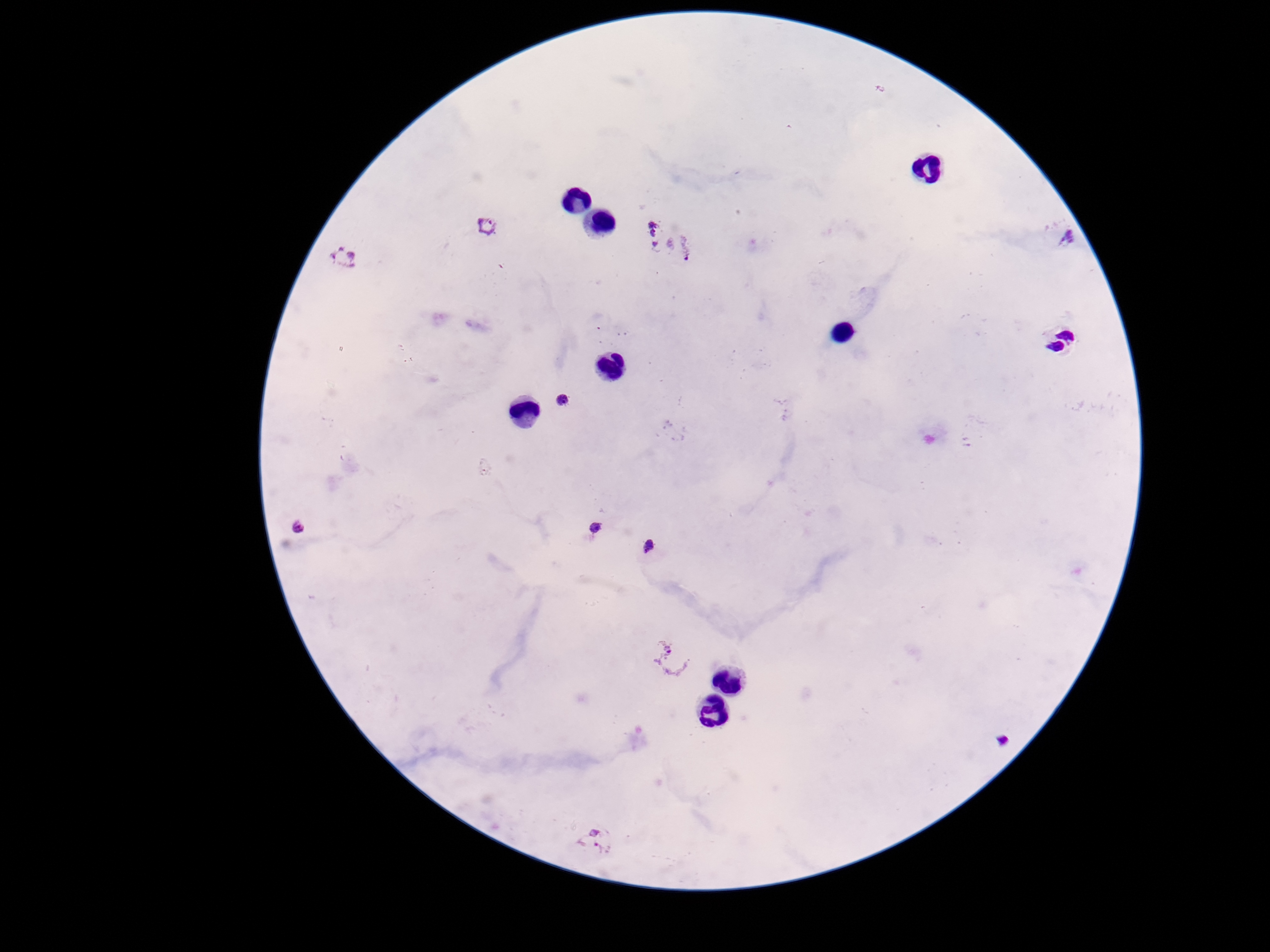

Approximate centers as [x, y] in pixels.
Summary:
  - Plasmodium parasite locations: [484, 229], [649, 230], [1068, 239], [687, 247], [342, 257], [567, 402], [297, 528], [598, 529], [649, 548], [678, 660], [1000, 735], [596, 842]
  - Capture: smartphone camera through the microscope eyepiece
  - Magnification: 100x
  - Preparation: thick blood smear
  - Field of view: one from this slide
  - Stain: Giemsa
  - Image size: 1270×952 pixels
  - Patient malaria status: infected